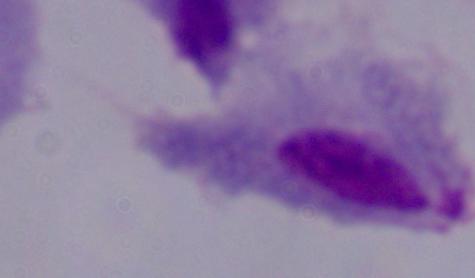
Summary:
  - Identification: trichomonad
  - Magnification: 1000x
  - Modality: photomicrograph